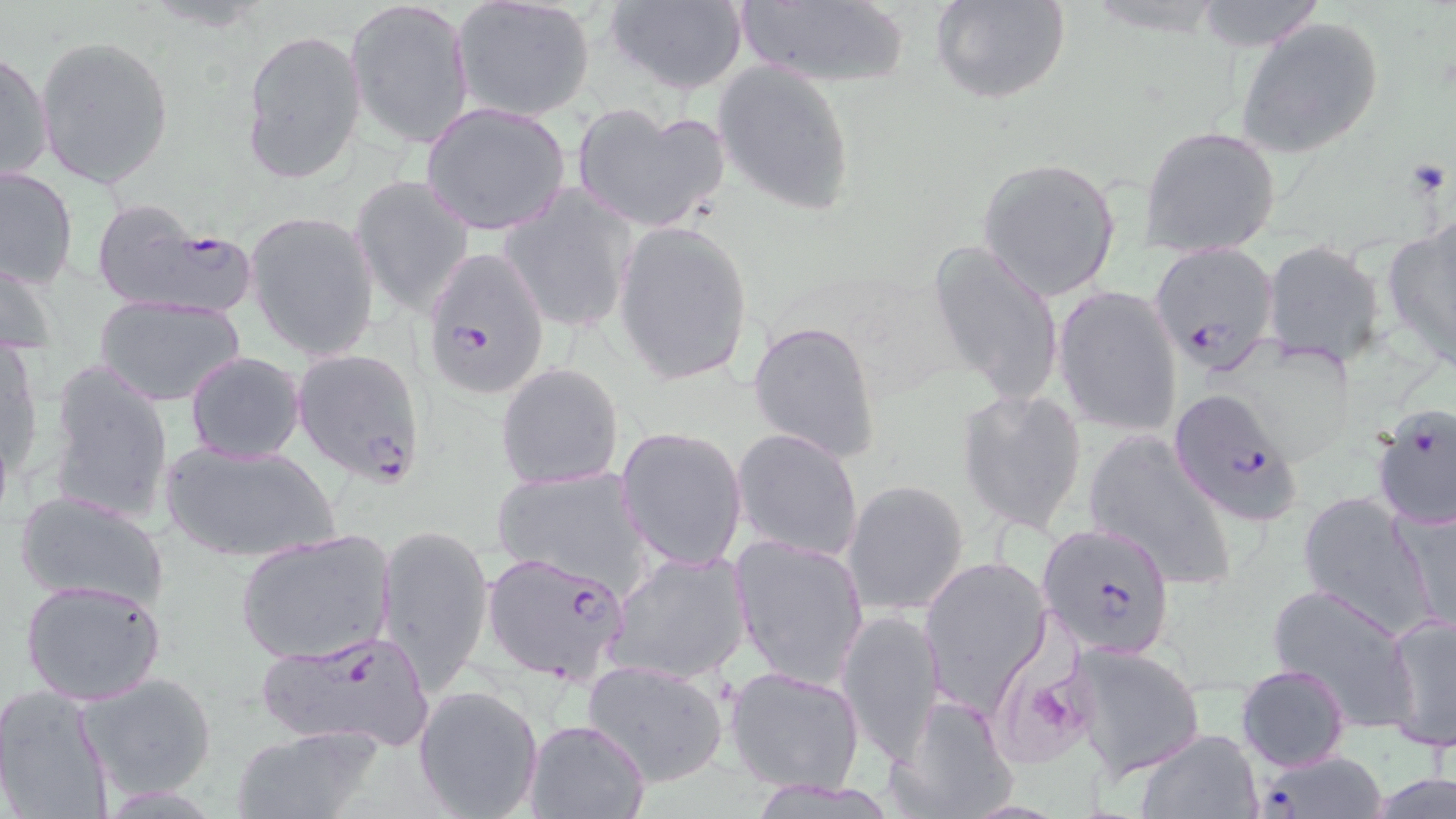
Approximate bounding boxes as [x1, y1, x2, y2] in pixels. Uninfected red blood cell locations: [346, 0, 474, 148], [604, 0, 748, 94], [733, 0, 910, 88], [933, 0, 1072, 105], [1191, 0, 1328, 51], [451, 1, 596, 122], [1235, 17, 1386, 161], [241, 29, 367, 183], [34, 34, 174, 189], [1, 48, 52, 186], [712, 60, 855, 214], [421, 102, 571, 236], [571, 103, 732, 234], [1139, 124, 1284, 260], [976, 156, 1122, 302], [0, 165, 78, 290], [352, 175, 475, 319], [502, 186, 636, 334], [246, 209, 380, 360], [613, 218, 754, 386], [1380, 219, 1456, 366], [927, 241, 1063, 408], [1261, 241, 1389, 371], [1, 254, 60, 358], [1055, 287, 1183, 436], [97, 296, 246, 405], [747, 317, 882, 464], [0, 338, 44, 480], [186, 351, 307, 462], [44, 360, 177, 526], [496, 362, 624, 490], [957, 386, 1089, 536], [617, 426, 748, 569], [732, 428, 865, 563], [1081, 428, 1238, 592], [159, 439, 341, 564], [492, 465, 652, 595], [842, 479, 970, 616], [14, 489, 171, 611], [1296, 490, 1442, 639], [1389, 500, 1456, 636], [375, 521, 495, 694], [235, 528, 397, 666], [731, 533, 871, 690], [607, 548, 753, 686], [918, 557, 1053, 710], [20, 577, 168, 706], [1267, 583, 1420, 732], [837, 608, 945, 767], [1383, 611, 1455, 752], [1067, 642, 1206, 779], [583, 660, 731, 787], [1236, 664, 1352, 771], [725, 665, 865, 794], [81, 671, 217, 799], [0, 684, 117, 818], [413, 684, 544, 819], [888, 694, 1017, 818], [525, 718, 651, 819], [229, 724, 387, 818], [1133, 728, 1261, 819], [1371, 773, 1456, 818]. Platelet locations: [1405, 156, 1452, 200], [996, 660, 1096, 763]. Plasmodium falciparum-infected red blood cell locations: [89, 199, 253, 319], [1149, 241, 1279, 376], [420, 244, 551, 401], [291, 346, 426, 486], [1162, 393, 1307, 523], [1370, 402, 1456, 532], [1037, 522, 1175, 659], [480, 551, 634, 684], [249, 631, 439, 751], [1252, 748, 1390, 819]. Slide-level diagnosis: Plasmodium falciparum. Image is 1456×819 pixels. Light microscopy. Captured at 1000x magnification. Thin blood film. May-Grünwald-Giemsa stain. One field of a larger specimen.